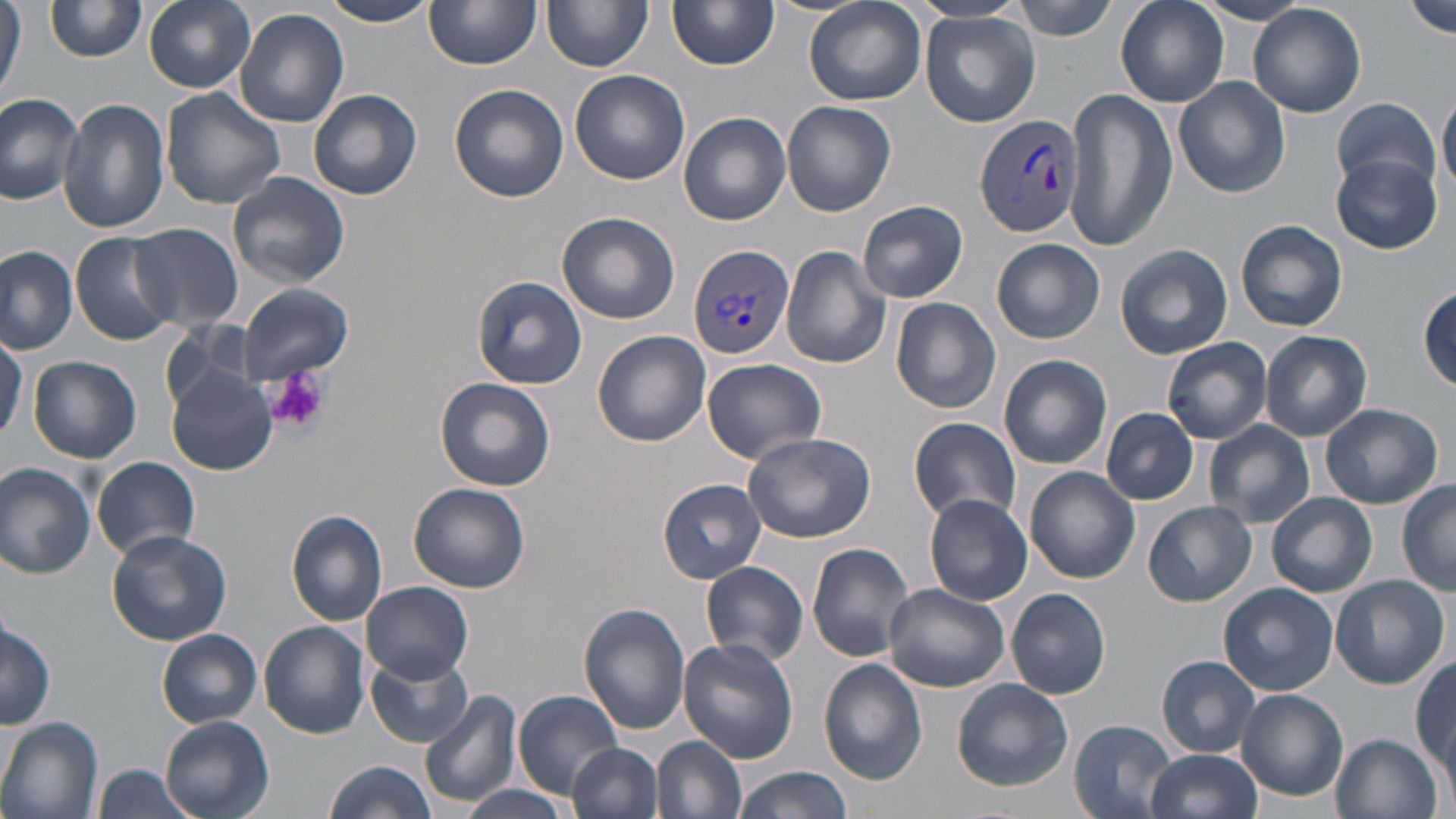 Approximate bounding boxes as [x1, y1, x2, y2] in pixels. Uninfected red blood cell locations: [0, 0, 25, 103], [45, 0, 148, 62], [145, 0, 255, 91], [323, 0, 434, 27], [668, 0, 779, 69], [910, 0, 1032, 24], [1010, 0, 1121, 40], [1115, 0, 1228, 107], [1402, 0, 1456, 38], [425, 1, 540, 70], [543, 1, 652, 73], [804, 1, 927, 107], [1195, 1, 1314, 26], [1248, 3, 1367, 118], [235, 8, 350, 128], [920, 13, 1040, 127], [569, 69, 690, 185], [1174, 76, 1290, 197], [450, 84, 569, 204], [161, 88, 286, 209], [1062, 88, 1176, 251], [308, 89, 422, 201], [1439, 90, 1456, 201], [0, 92, 85, 203], [1332, 96, 1439, 193], [58, 98, 171, 235], [781, 101, 896, 216], [678, 112, 792, 225], [1332, 155, 1443, 253], [227, 171, 351, 289], [858, 200, 968, 304], [557, 211, 680, 325], [1236, 220, 1348, 331], [129, 223, 243, 331], [74, 232, 183, 345], [992, 238, 1103, 343], [1114, 243, 1232, 359], [779, 245, 892, 369], [0, 246, 77, 352], [473, 275, 586, 390], [236, 283, 351, 383], [1419, 284, 1456, 391], [891, 296, 1002, 413], [161, 322, 262, 412], [0, 330, 26, 444], [593, 330, 712, 446], [1260, 331, 1372, 440], [1162, 337, 1272, 443], [997, 355, 1112, 468], [28, 356, 142, 462], [701, 356, 826, 464], [166, 367, 278, 476], [435, 376, 557, 492], [1320, 403, 1441, 509], [1101, 407, 1199, 504], [909, 416, 1021, 525], [1204, 419, 1315, 528], [742, 432, 875, 543], [92, 456, 200, 563], [0, 464, 95, 580], [1025, 466, 1140, 583], [657, 478, 766, 583], [1396, 482, 1456, 595], [408, 483, 530, 593], [1268, 492, 1377, 596], [923, 494, 1032, 605], [1144, 500, 1257, 607], [286, 510, 389, 628], [106, 527, 233, 646], [807, 543, 915, 660], [700, 560, 810, 669], [1329, 575, 1449, 690], [363, 582, 473, 682], [884, 582, 1009, 692], [1218, 583, 1338, 694], [1006, 587, 1112, 699], [579, 603, 689, 735], [0, 616, 55, 731], [260, 621, 370, 738], [157, 630, 262, 727], [678, 639, 799, 764], [367, 653, 475, 748], [1156, 656, 1262, 757], [1412, 656, 1456, 776], [818, 658, 929, 786], [953, 678, 1073, 791], [1238, 688, 1349, 801], [419, 689, 520, 810], [513, 689, 626, 796], [160, 715, 274, 819], [1, 718, 104, 819], [1070, 719, 1176, 819], [1330, 732, 1443, 819], [654, 736, 749, 819], [571, 741, 664, 819], [1145, 749, 1263, 819], [322, 762, 439, 819], [94, 763, 198, 819], [732, 765, 851, 819], [458, 783, 577, 819]. Plasmodium vivax-infected red blood cell locations: [975, 115, 1087, 241], [689, 244, 795, 358]. Platelet locations: [269, 367, 328, 432]. Slide-level diagnosis: Plasmodium vivax. One field of a larger specimen. Optical microscopy. 1000x magnification. Image is 1456×819 pixels. Thin blood film. May-Grünwald-Giemsa stain.